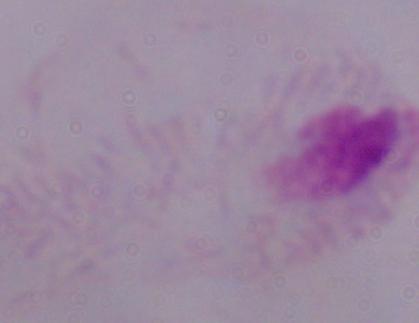 Captured at 1000x magnification. Photomicrograph. A trichomonad is shown.